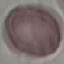

Malaria status: uninfected. Giemsa-stained preparation. Acquired by smartphone through the microscope eyepiece. Automatically extracted cell patch, resized to 64 × 64 pixels. Thin blood film.